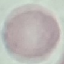

result = no malaria parasites seen
image type = automatically extracted cell patch, resized to 64 × 64 pixels
stain = Giemsa
capture = smartphone camera at the microscope eyepiece
preparation = thin blood smear